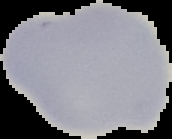

preparation = thin blood smear
malaria status = uninfected
image size = 172×139 pixels
image type = segmented cell region with the area outside set to black